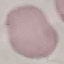
Malaria status: uninfected. Giemsa stain. Cell patch, automatically extracted from a larger field of view and resized to 64 × 64 pixels. Thin blood smear. Acquired by smartphone through the microscope eyepiece.